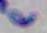
1000x magnification. Toxoplasma gondii is seen. Micrograph.